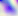

Summary:
  - Magnification: 400x
  - Identification: Toxoplasma gondii
  - Modality: micrograph